State which parasite is depicted.
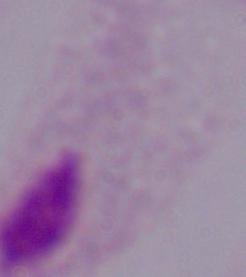

A trichomonad.

Summary:
  - Magnification: 1000x
  - Modality: photomicrograph